Describe the morphology of the erythrocytes.
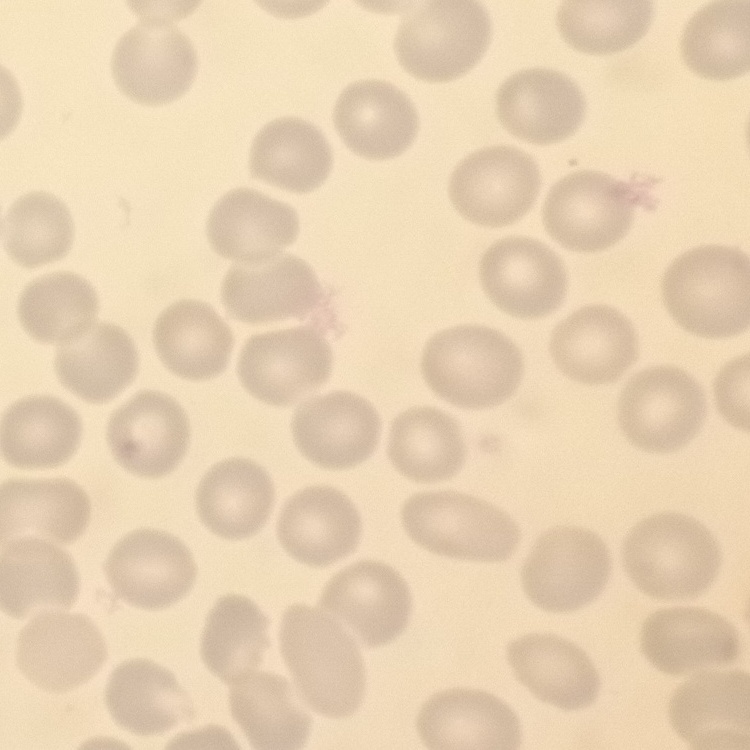

No rouleaux formation.

image type = square crop of a larger photomicrograph
preparation = thin peripheral smear
stain = Field's or Giemsa